Describe the morphology of the red blood cells.
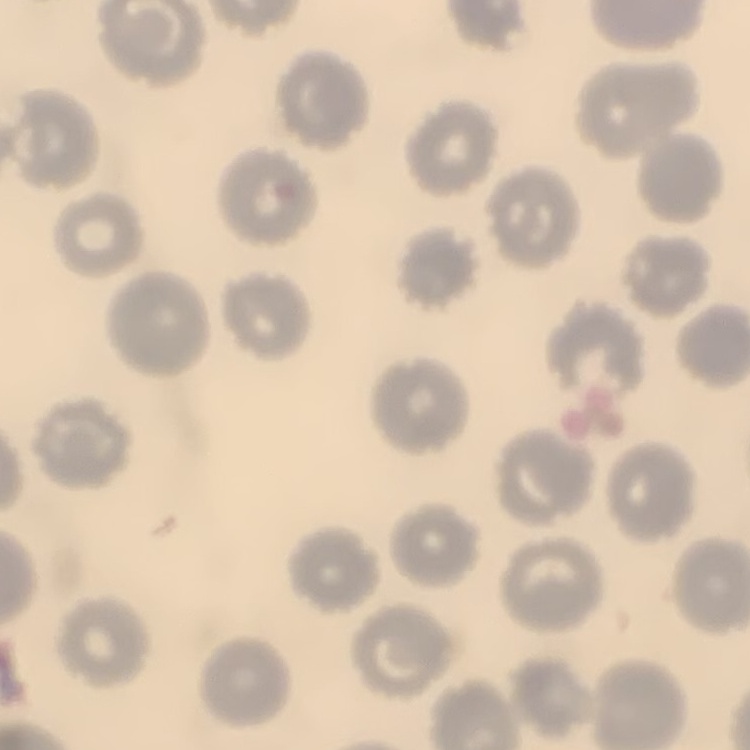
No rouleaux formation.

Summary:
  - Preparation: thin blood smear
  - Image type: one tile cut from a larger photomicrograph
  - Stain: Field's or Giemsa